State which parasite is depicted.
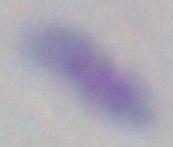

Toxoplasma gondii.

Micrograph. 1000x magnification.